Give the position of every Plasmodium parasite visible.
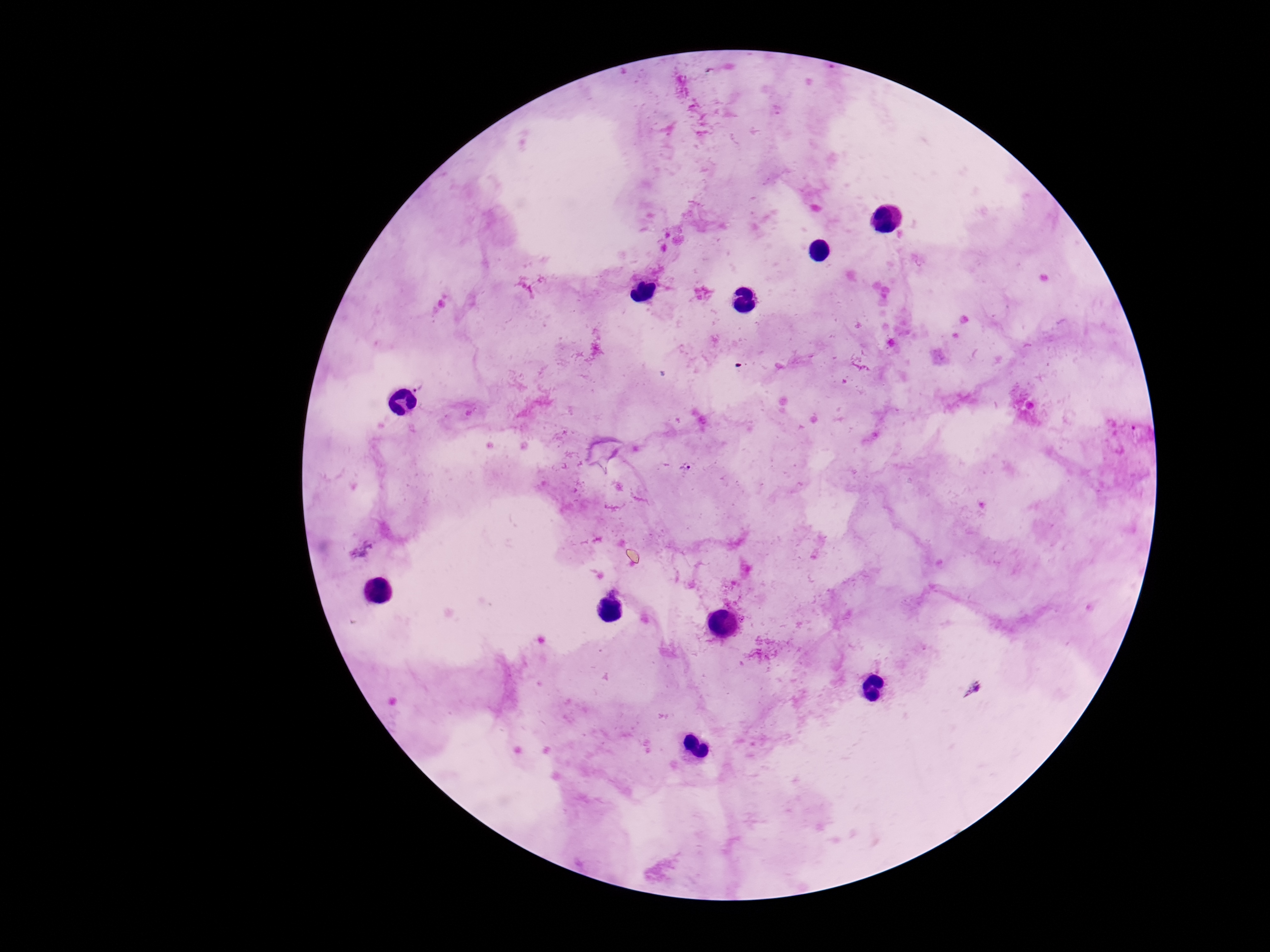
Approximate object centers, in pixels from the top-left corner.
Plasmodium parasites: (x=419, y=381), (x=690, y=465).

Summary:
  - Capture: smartphone camera through the microscope eyepiece
  - Image size: 1270×952 pixels
  - Stain: Giemsa
  - Preparation: thick peripheral-blood smear
  - Patient malaria status: positive
  - Field of view: one from this slide
  - Magnification: 100x